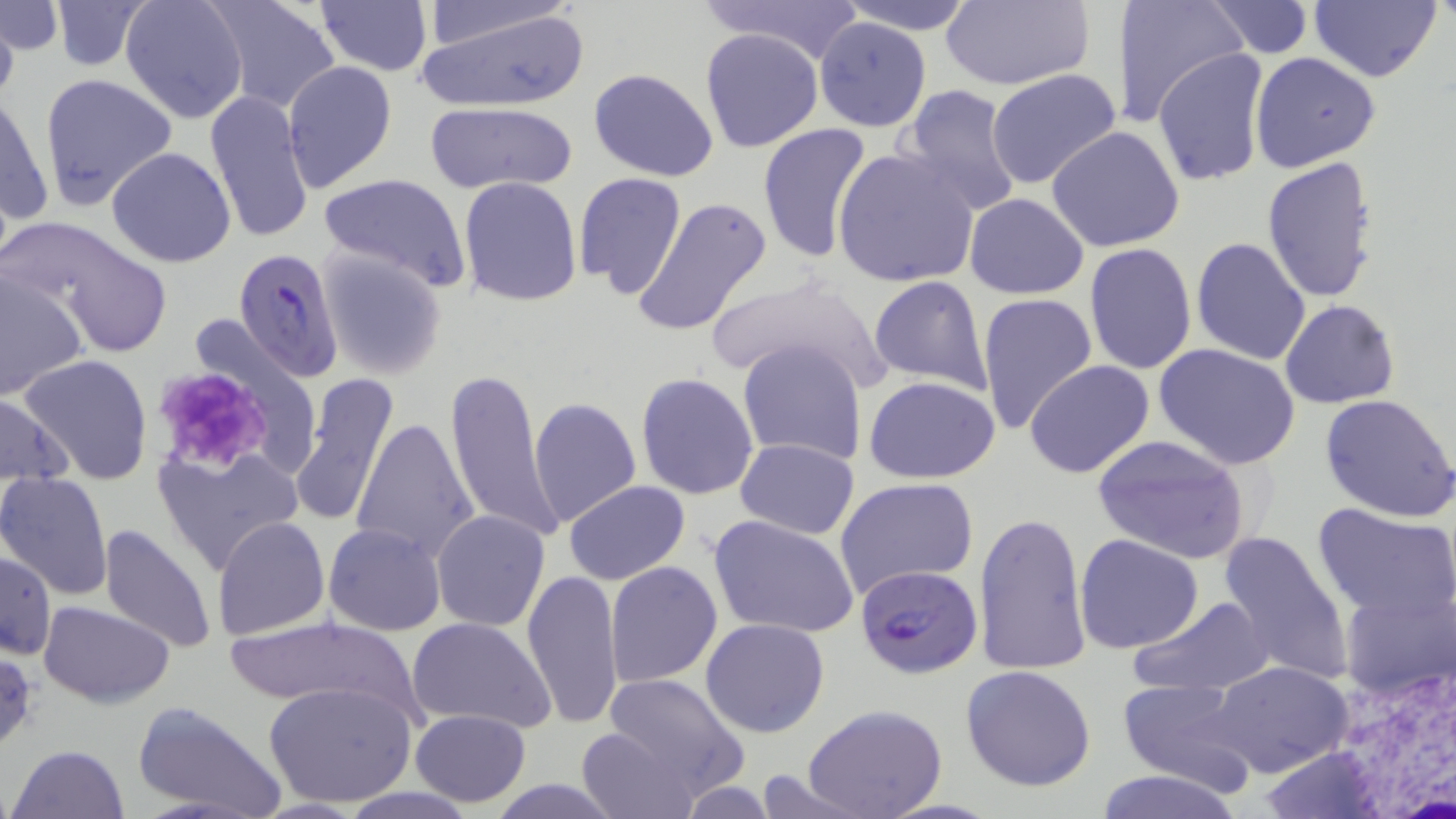
Approximate bounding boxes as [x1, y1, x2, y2] in pixels. Uninfected red blood cell locations: [120, 0, 251, 124], [205, 0, 341, 113], [698, 0, 867, 66], [836, 0, 977, 34], [938, 0, 1093, 90], [1123, 0, 1245, 127], [1308, 0, 1442, 83], [48, 1, 155, 73], [315, 1, 432, 77], [413, 1, 591, 110], [416, 1, 577, 54], [1201, 1, 1316, 57], [0, 2, 62, 53], [0, 11, 18, 113], [813, 17, 931, 133], [699, 28, 824, 153], [1153, 48, 1270, 188], [1250, 52, 1381, 173], [283, 60, 396, 191], [589, 68, 720, 181], [986, 69, 1124, 192], [39, 72, 178, 209], [898, 85, 1025, 218], [204, 89, 315, 245], [0, 92, 53, 237], [422, 102, 577, 197], [757, 122, 874, 263], [1047, 125, 1186, 253], [106, 146, 236, 266], [833, 147, 980, 288], [1261, 158, 1382, 305], [317, 172, 472, 294], [573, 172, 687, 298], [458, 177, 582, 305], [964, 194, 1089, 299], [632, 196, 773, 337], [6, 218, 170, 358], [1190, 237, 1311, 366], [1084, 243, 1197, 375], [315, 249, 449, 380], [0, 268, 88, 402], [702, 274, 891, 388], [867, 276, 992, 394], [976, 293, 1098, 438], [1280, 299, 1400, 408], [738, 338, 869, 463], [1155, 342, 1301, 469], [19, 353, 152, 484], [1024, 360, 1155, 479], [443, 365, 566, 546], [288, 372, 399, 528], [636, 373, 760, 499], [864, 376, 1001, 484], [0, 393, 75, 487], [1321, 393, 1456, 522], [527, 396, 642, 530], [352, 418, 480, 564], [1092, 434, 1251, 563], [734, 438, 859, 538], [152, 444, 302, 576], [0, 471, 113, 599], [835, 477, 979, 599], [563, 481, 691, 583], [1313, 504, 1456, 622], [431, 510, 551, 633], [974, 510, 1090, 676], [709, 514, 860, 638], [210, 516, 330, 641], [98, 522, 217, 655], [323, 523, 446, 635], [1215, 528, 1355, 686], [1075, 534, 1204, 655], [1, 552, 55, 660], [605, 560, 723, 686], [522, 569, 624, 730], [1340, 585, 1453, 705], [1128, 594, 1277, 699], [39, 600, 175, 707], [223, 616, 421, 716], [405, 617, 556, 732], [701, 618, 830, 738], [1211, 660, 1355, 779], [960, 664, 1097, 791], [603, 673, 749, 795], [1117, 678, 1256, 791], [264, 680, 418, 807], [131, 702, 284, 818], [802, 703, 949, 819], [410, 708, 530, 808], [574, 725, 698, 819], [1255, 741, 1392, 817], [9, 744, 128, 819], [1092, 769, 1245, 819], [742, 770, 875, 817], [486, 780, 625, 816]. Platelet locations: [149, 366, 273, 471]. Plasmodium falciparum-infected red blood cell locations: [234, 247, 344, 382], [855, 565, 982, 680]. White blood cell locations: [1328, 669, 1456, 815]. Slide-level diagnosis: Plasmodium falciparum. Optical microscopy. 1000x magnification. Single field of view. Thin blood film. May-Grünwald-Giemsa stain. Image is 1456×819 pixels.